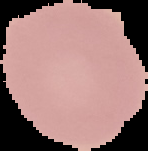
Summary:
  - Image size: 148×151 pixels
  - Result: no Plasmodium parasites seen
  - Preparation: thin blood film
  - Image type: segmented cell region on a black background